Name the parasite shown.
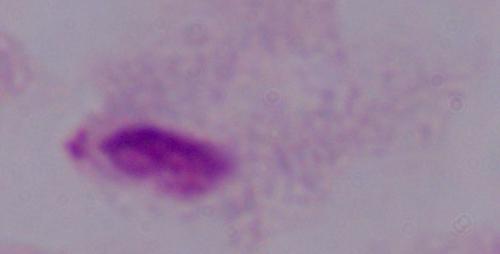

A trichomonad.

Summary:
  - Magnification: 1000x
  - Modality: micrograph